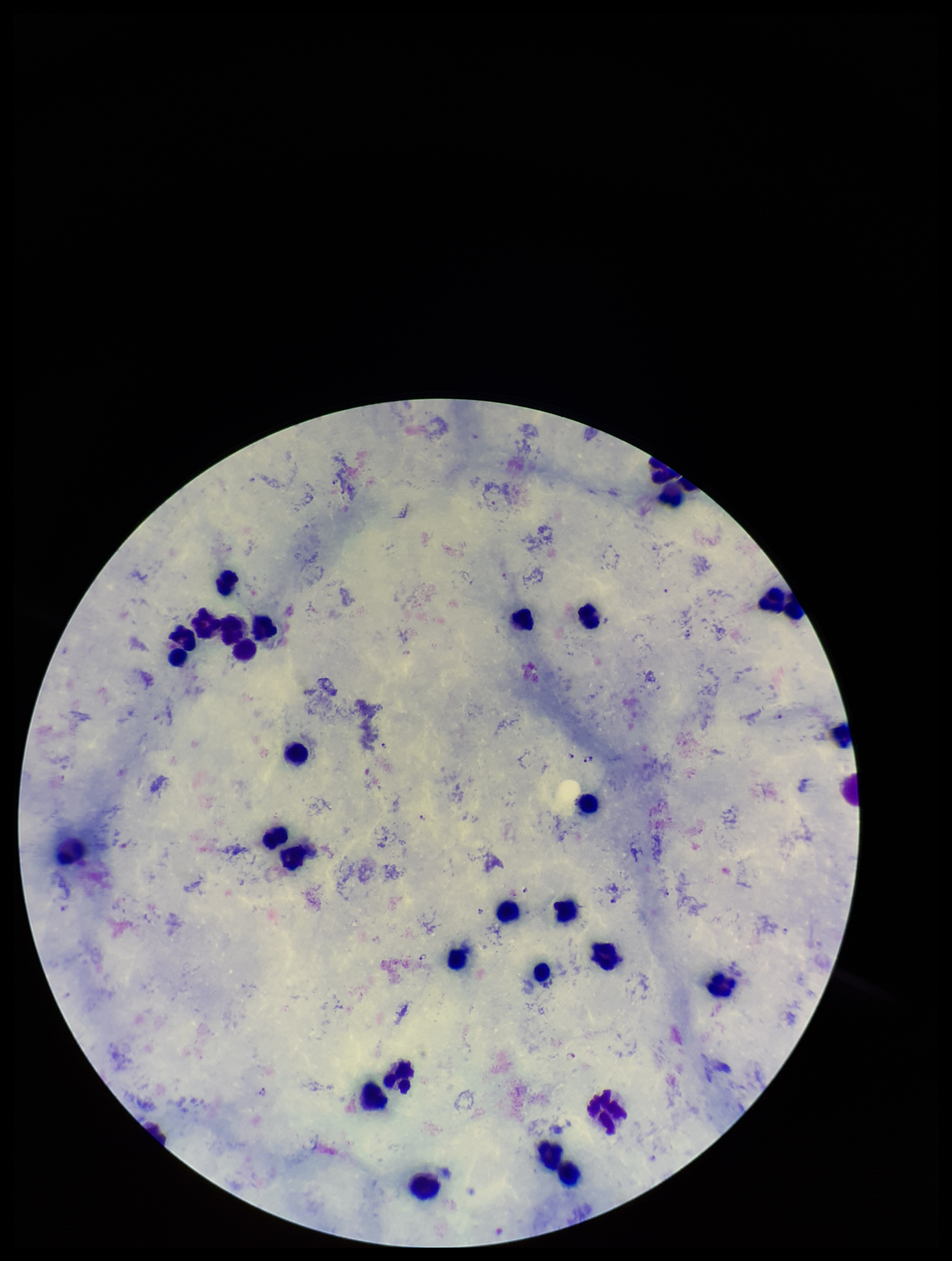

One field from this slide. Leukocyte count: 31. Patient malaria status: positive. Image is 952×1261 pixels. Plasmodium parasites: seen. Parasite count: 18. Preparation: thick. Photographed through the microscope eyepiece with a smartphone camera. Stained with Giemsa. Species reported for this patient: Plasmodium falciparum.